Classify this cell by malaria status.
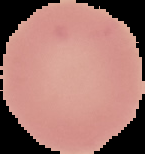

It is uninfected.

Cell region segmented out of the field of view; the surrounding area is masked to black. From a thin blood film. Image is 145×154 pixels.